Classify this cell by malaria status.
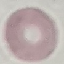

It is uninfected.

Summary:
  - Capture: smartphone through the microscope eyepiece
  - Preparation: thin blood film
  - Stain: Giemsa
  - Image type: cell patch, automatically extracted from a larger field of view and resized to 64 × 64 pixels